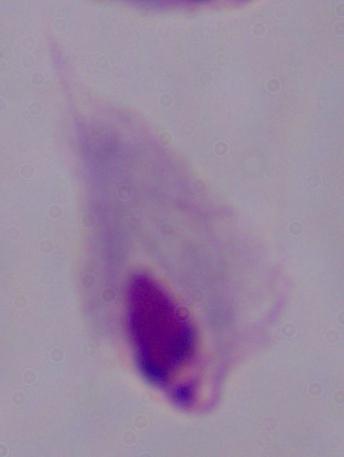

Summary:
  - Magnification: 1000x
  - Modality: photomicrograph
  - Identification: trichomonad